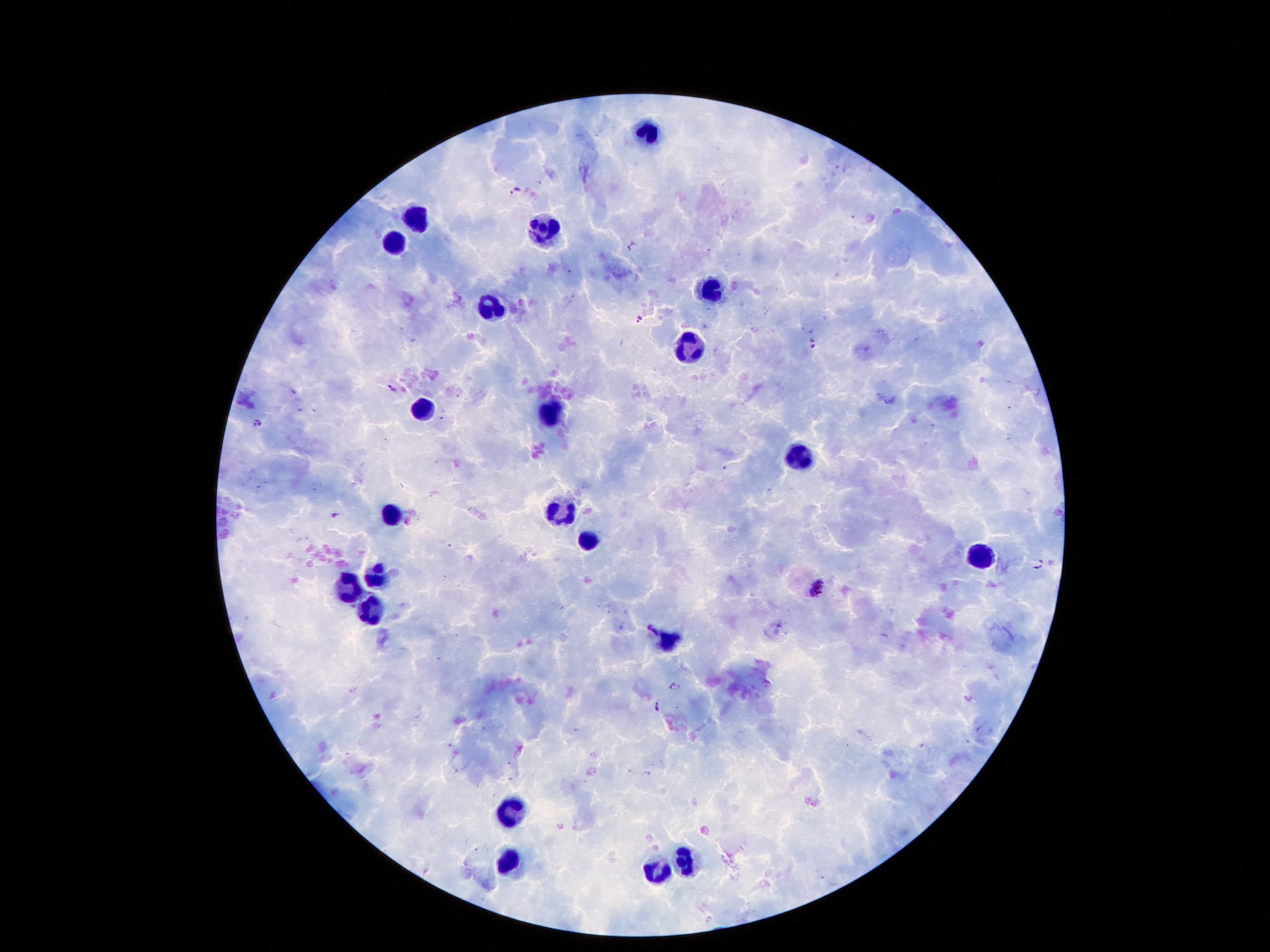 Approximate centers as {x, y} in pixels. Leukocyte locations: {649, 131}, {418, 219}, {547, 227}, {395, 241}, {710, 290}, {487, 307}, {692, 350}, {418, 409}, {545, 416}, {795, 455}, {564, 511}, {393, 517}, {587, 541}, {983, 557}, {379, 575}, {351, 586}, {372, 609}, {668, 642}, {513, 810}, {513, 859}, {685, 859}, {656, 872}. Malaria parasite locations: {515, 191}, {633, 246}, {639, 319}, {814, 345}, {392, 387}, {258, 423}, {336, 514}, {1040, 564}, {817, 588}, {675, 687}, {657, 707}. Thick peripheral-blood smear. Single field of view. Photographed through the microscope eyepiece with a smartphone camera. Giemsa-stained preparation. Patient malaria status: positive for Plasmodium falciparum. Image is 1270×952 pixels. 100x magnification.